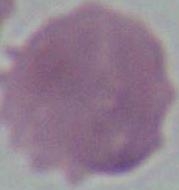

identification = red blood cell
magnification = 1000x
modality = micrograph